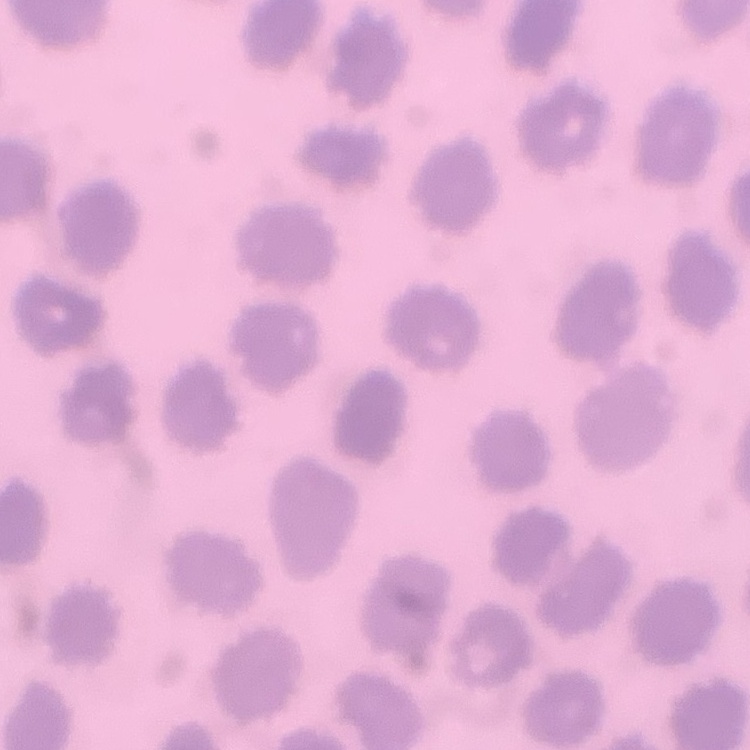
The red blood cells exhibit no rouleaux formation. Field's or Giemsa stain. Square crop of a larger photomicrograph. Thin blood smear.